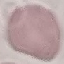
result = no malaria parasites detected
capture = smartphone through the microscope eyepiece
image type = cell patch, automatically extracted from a larger field of view and resized to 64 × 64 pixels
preparation = thin blood film
stain = Giemsa